Assess this cell for malaria.
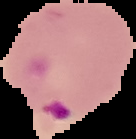

Parasitized.

Summary:
  - Preparation: thin blood smear
  - Image size: 136×139 pixels
  - Image type: segmented cell region with the area outside set to black